State the blood parasite species.
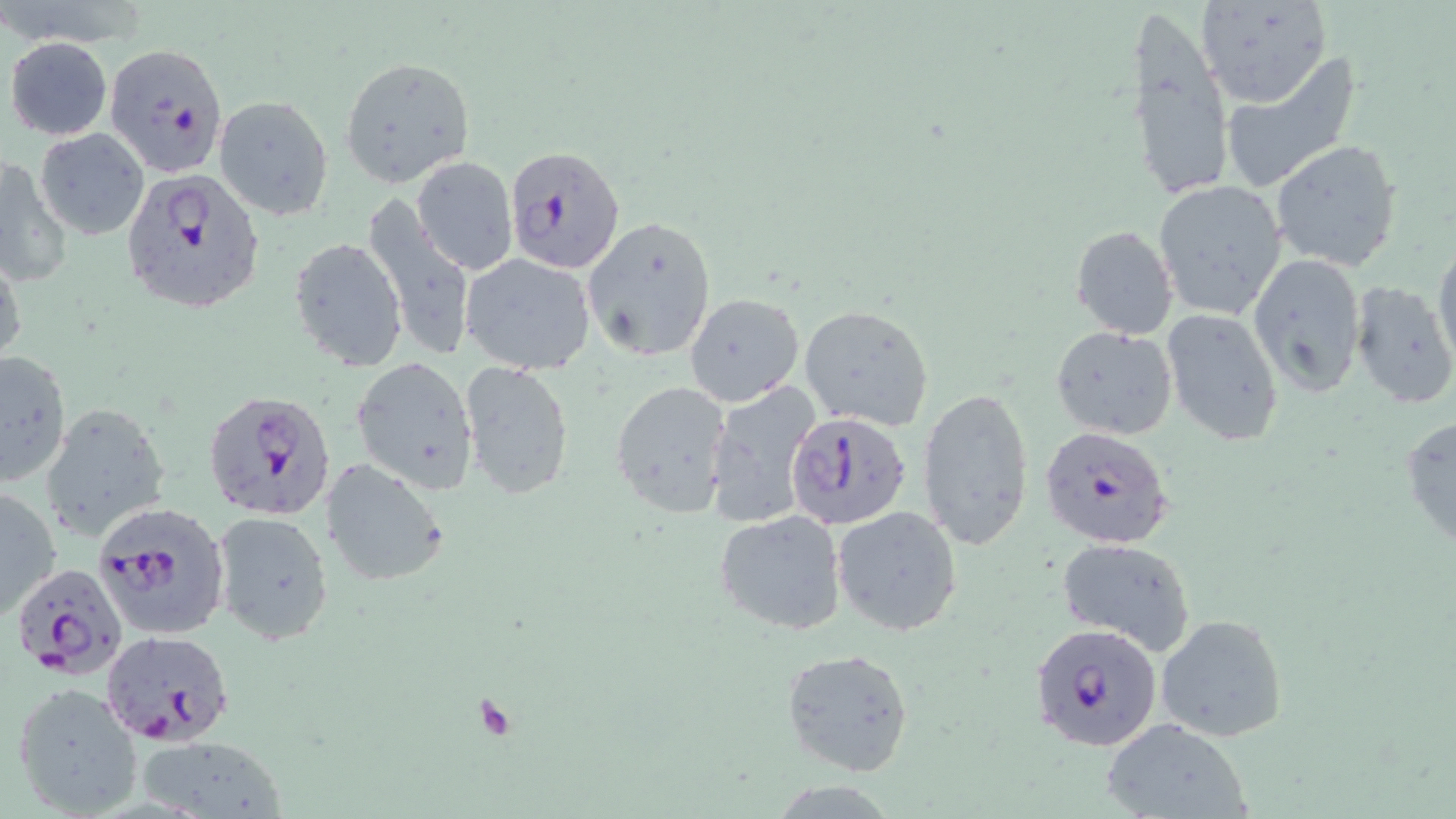

Plasmodium falciparum.

Approximate bounding boxes as (x1, y1, x2, y2) in pixels. Plasmodium falciparum-infected red blood cell locations: (101, 39, 225, 177), (503, 143, 623, 275), (120, 169, 265, 314), (205, 390, 336, 521), (785, 413, 912, 532), (1042, 426, 1172, 548), (93, 502, 231, 642), (23, 560, 130, 684), (1029, 621, 1163, 755), (101, 631, 236, 748). Uninfected red blood cell locations: (1196, 1, 1333, 109), (1125, 11, 1234, 204), (4, 36, 112, 138), (1219, 55, 1364, 195), (339, 56, 475, 187), (214, 93, 333, 220), (34, 128, 149, 241), (1268, 140, 1403, 271), (411, 155, 518, 275), (0, 156, 69, 289), (1152, 179, 1287, 320), (361, 197, 474, 362), (581, 213, 718, 364), (1070, 224, 1179, 340), (1433, 235, 1456, 372), (289, 236, 408, 372), (1247, 251, 1367, 398), (0, 253, 26, 374), (461, 253, 595, 375), (1349, 280, 1455, 410), (684, 291, 805, 408), (798, 304, 934, 430), (1161, 308, 1285, 445), (1051, 326, 1178, 439), (0, 349, 71, 488), (352, 355, 481, 494), (461, 361, 574, 499), (611, 379, 733, 519), (705, 380, 822, 528), (918, 385, 1035, 550), (45, 401, 174, 542), (1400, 412, 1456, 558), (321, 457, 450, 588), (0, 484, 62, 623), (831, 505, 963, 637), (212, 511, 334, 644), (714, 511, 848, 636), (1057, 538, 1196, 655), (1157, 612, 1289, 743), (781, 648, 915, 778), (11, 680, 146, 819), (1099, 718, 1252, 819), (134, 733, 287, 818). Platelet locations: (473, 695, 521, 744). Thin blood smear. Light microscopy. May-Grünwald-Giemsa stain. Captured at 1000x magnification. Image is 1456×819 pixels. Single field of view.